Report the malaria status of this cell.
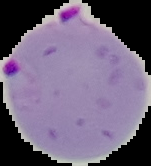
It is parasitized.

Segmented cell region on a black background. From a thin blood smear. Image is 151×166 pixels.